Classify this cell by malaria status.
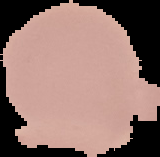
It is uninfected.

From a thin blood film. The area outside the segmented cell region is set to black. Image is 160×157 pixels.